State the blood parasite species.
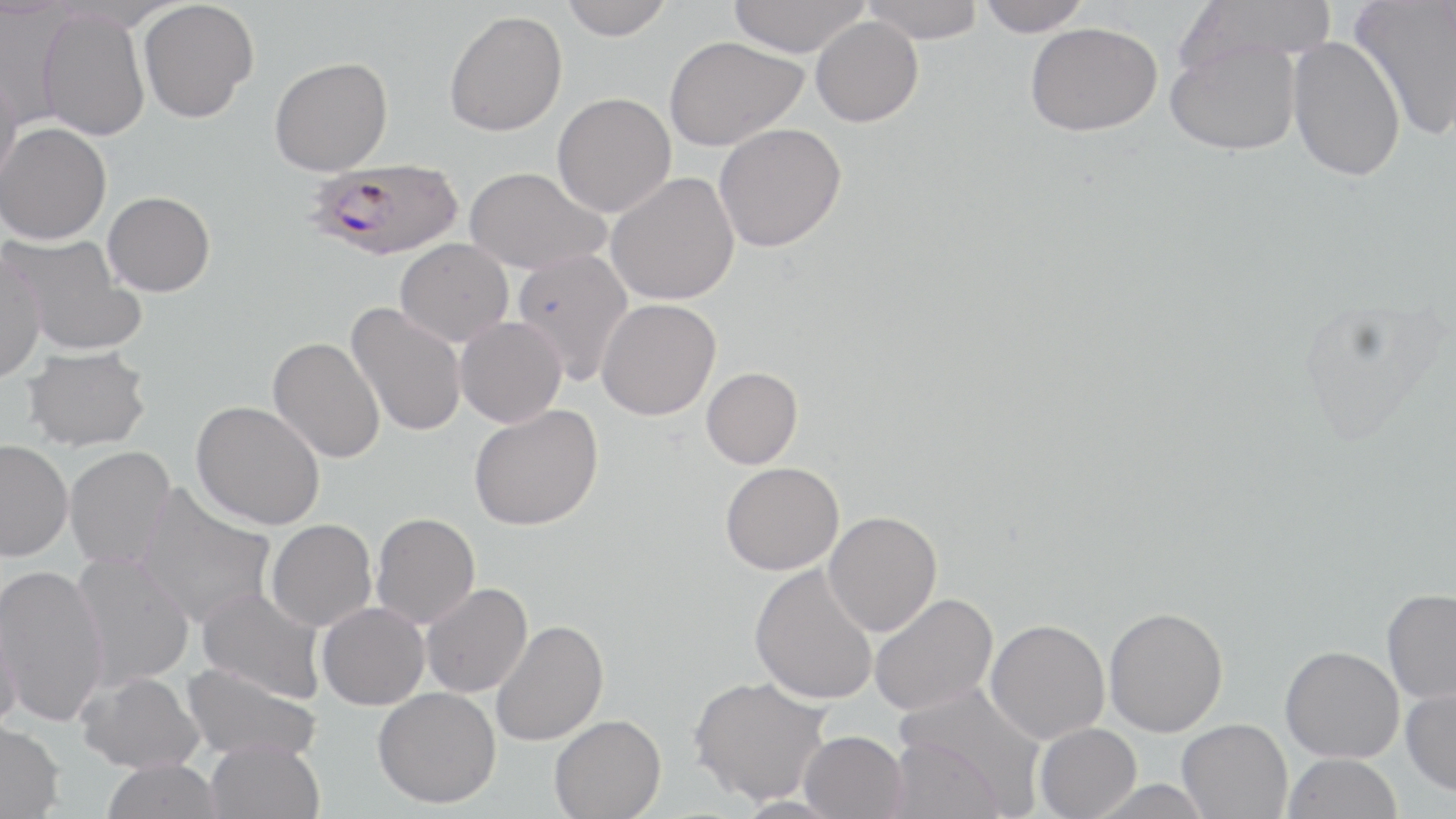

Plasmodium falciparum.

Approximate bounding boxes as [x1, y1, x2, y2] in pixels. Plasmodium falciparum-infected red blood cell locations: [303, 159, 465, 260]. Uninfected red blood cell locations: [560, 0, 673, 40], [728, 0, 869, 57], [860, 0, 986, 42], [976, 0, 1091, 37], [1179, 0, 1337, 71], [1350, 0, 1456, 142], [138, 1, 258, 123], [36, 9, 151, 141], [443, 10, 567, 136], [810, 16, 923, 127], [1024, 22, 1162, 136], [663, 35, 808, 151], [1287, 35, 1406, 182], [1164, 37, 1301, 156], [269, 56, 393, 176], [0, 69, 22, 190], [551, 93, 676, 217], [0, 123, 111, 245], [712, 123, 845, 252], [463, 166, 610, 275], [605, 172, 740, 305], [102, 191, 215, 296], [2, 232, 144, 358], [394, 238, 513, 346], [511, 248, 634, 384], [0, 249, 46, 383], [596, 299, 720, 420], [345, 304, 467, 438], [454, 316, 567, 428], [268, 336, 385, 464], [22, 345, 151, 452], [701, 366, 803, 468], [191, 400, 325, 530], [469, 403, 603, 531], [0, 439, 73, 561], [63, 446, 175, 569], [720, 462, 844, 575], [134, 484, 277, 630], [823, 511, 941, 636], [371, 513, 480, 629], [265, 519, 377, 631], [70, 551, 194, 690], [749, 562, 878, 705], [0, 564, 108, 727], [420, 583, 532, 698], [196, 587, 326, 703], [1381, 588, 1456, 704], [869, 592, 997, 715], [316, 602, 429, 710], [0, 605, 23, 732], [1103, 606, 1228, 736], [491, 619, 608, 746], [985, 619, 1110, 743], [1280, 645, 1404, 762], [181, 662, 321, 762], [77, 671, 206, 774], [688, 676, 831, 806], [894, 682, 1048, 809], [372, 686, 501, 808], [1401, 686, 1456, 795], [549, 714, 666, 818], [1177, 717, 1292, 818], [0, 719, 66, 818], [1034, 723, 1141, 819], [799, 730, 908, 819], [885, 736, 1009, 819], [205, 739, 324, 819], [1282, 752, 1403, 819], [101, 758, 223, 819], [1087, 779, 1213, 819]. May-Grünwald-Giemsa-stained preparation. Captured at 1000x magnification. Thin blood smear. Single field of view. Light microscopy. Image is 1456×819 pixels.